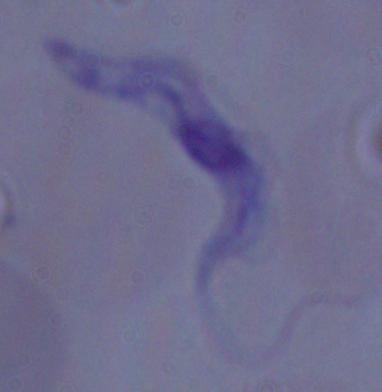
modality = micrograph
identification = trypanosome
magnification = 1000x